Point out each Plasmodium parasite.
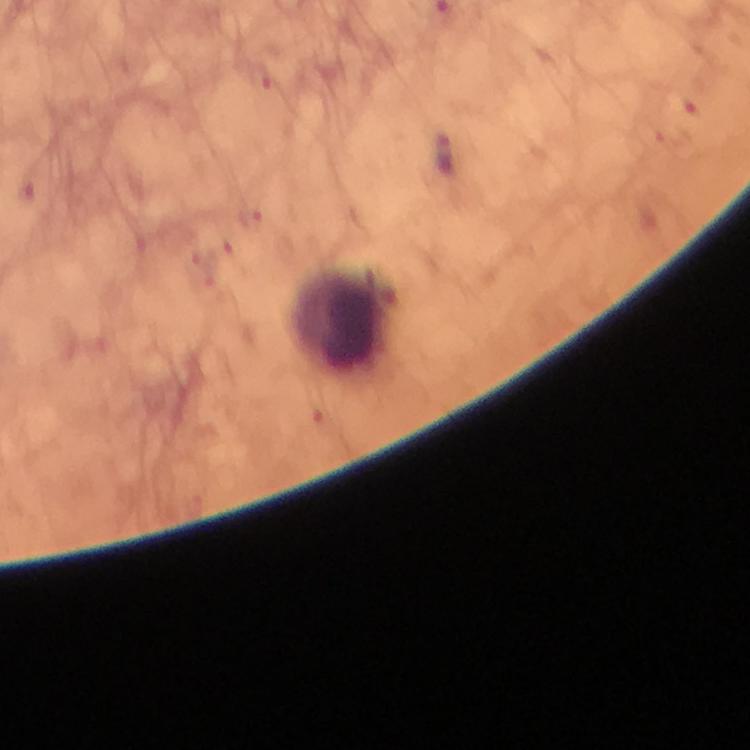
Approximate centers as {x, y} in pixels.
Plasmodium parasites: {444, 153}.

Leukocyte locations: {339, 322}. 100x magnification. Immersion oil applied. Giemsa-stained preparation. From a diagnostic examination for malaria. A crop from one field of view. Photographed through the microscope with a smartphone camera. Thick blood film. Image is 750×750 pixels.